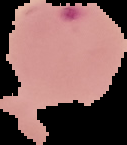

Summary:
  - Image size: 127×145 pixels
  - Preparation: thin blood smear
  - Image type: segmented cell region on a black background
  - Malaria status: parasitized